Locate every leukocyte (white blood cell).
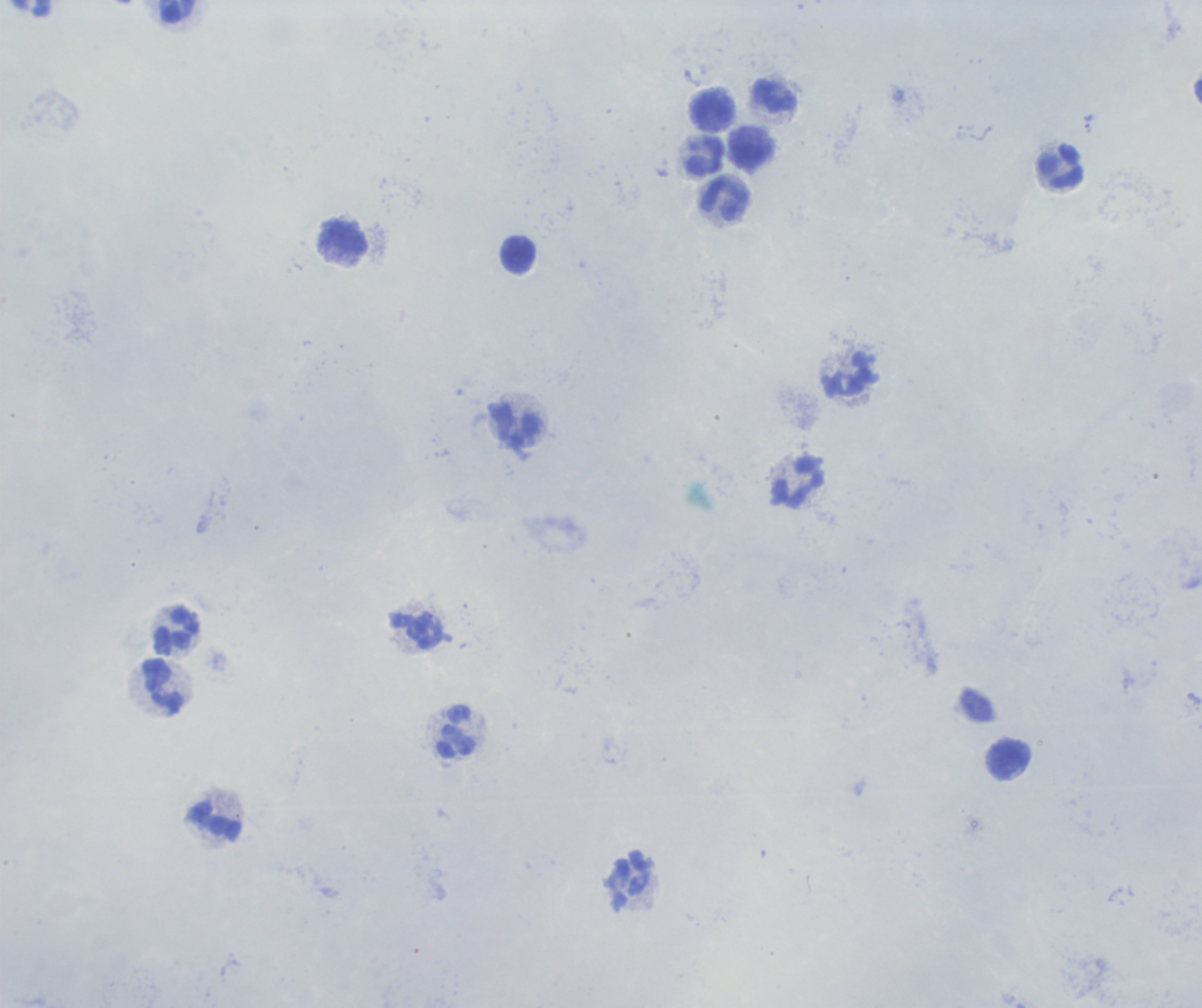
Approximate centers as (x, y) in pixels.
Leukocytes: (177, 11), (774, 97), (712, 108), (703, 155), (750, 156), (1061, 166), (726, 199), (345, 238), (518, 255), (852, 375), (516, 426), (800, 483), (417, 631), (178, 632), (163, 685), (456, 732), (1008, 759), (215, 822).

coordinate format = approximate centers as (x, y) in pixels
trophozoite locations = (1089, 123)
stain = Romanowsky
context = previously used in an actual diagnosis
magnification = 100x
image size = 1202×1008 pixels
field of view = single
preparation = thick blood smear
background quality = poor
result = positive for Plasmodium parasites